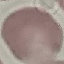
Summary:
  - Result: negative for malaria parasites
  - Image type: cell patch, automatically extracted from a larger field of view and resized to 64 × 64 pixels
  - Stain: Giemsa
  - Capture: smartphone through the microscope eyepiece
  - Preparation: thin blood film